Report the malaria status of this cell.
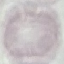
Uninfected.

Summary:
  - Preparation: thin blood smear
  - Stain: Giemsa
  - Capture: smartphone camera at the microscope eyepiece
  - Image type: cell patch, automatically extracted from a larger field of view and resized to 64 × 64 pixels